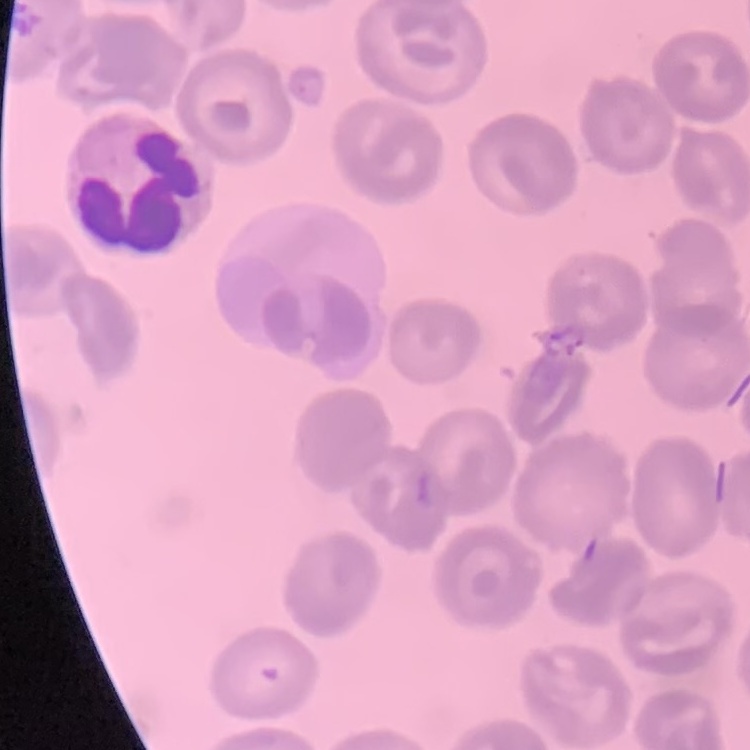

Summary:
  - Red blood cell morphology: no rouleaux formation
  - Preparation: thin peripheral smear
  - Stain: Field's or Giemsa
  - Image type: one tile cut from a larger photomicrograph